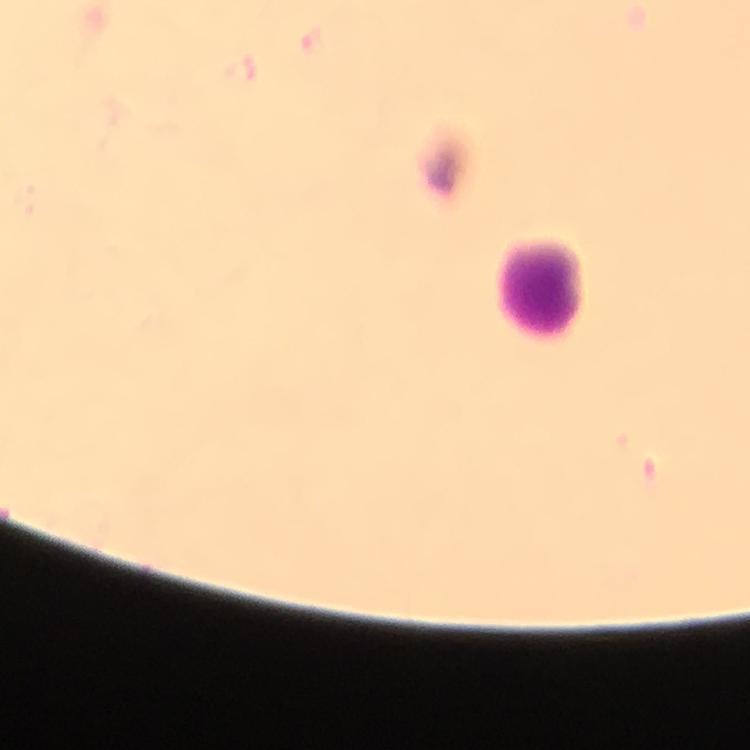

Approximate object centers, in pixels from the top-left corner.
Summary:
  - Leukocyte locations: (x=543, y=287)
  - Preparation: thick blood film
  - Context: from a malaria diagnostic workup
  - Malaria parasites: none detected
  - Immersion oil: used
  - Cropped from: a single field of view
  - Image size: 750×750 pixels
  - Stain: Giemsa
  - Capture: smartphone mounted on the microscope
  - Magnification: 100x